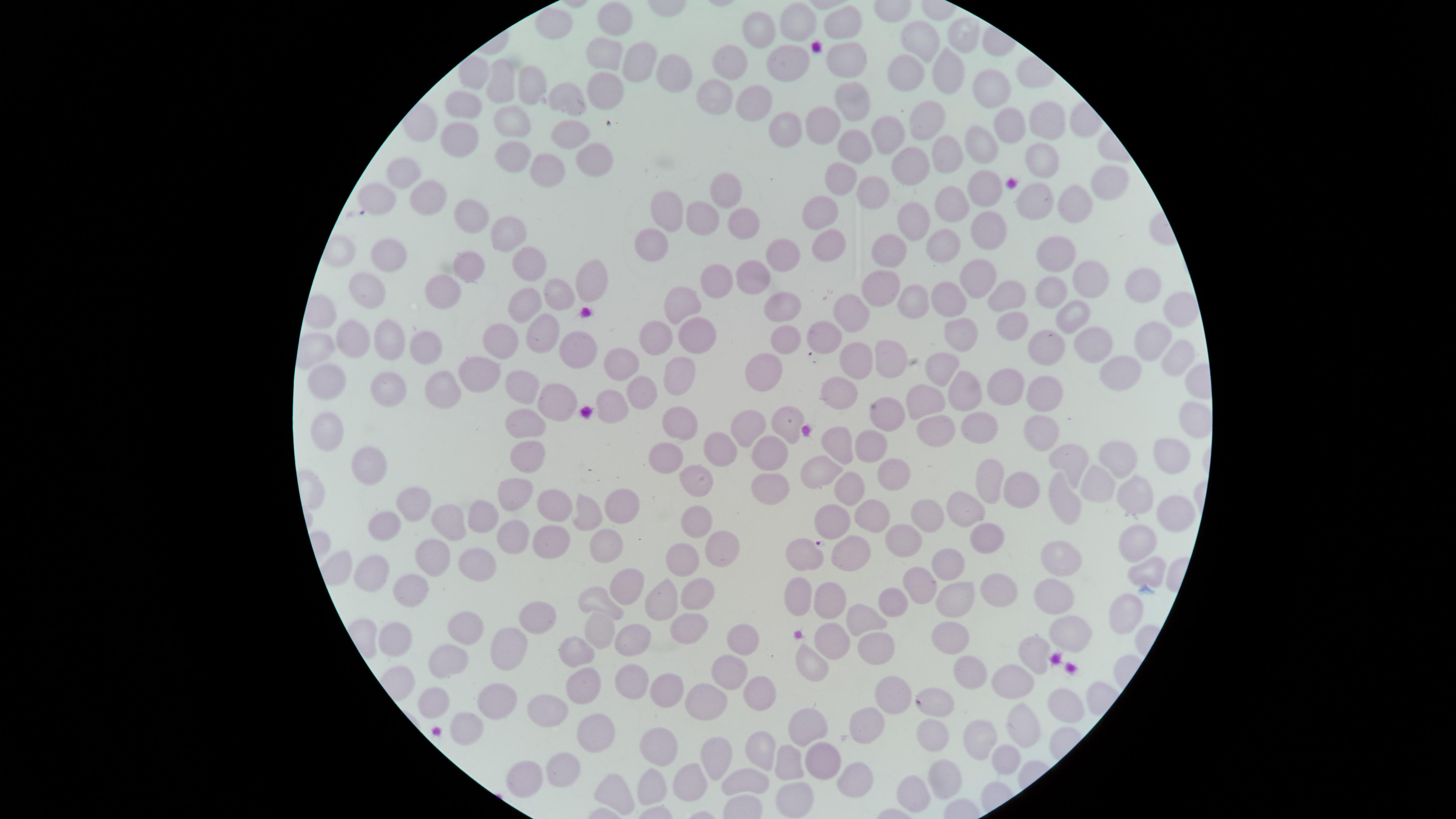 Approximate marker points as [x, y] in pixels. Uninfected red blood cells: [619, 19], [796, 21], [845, 22], [554, 27], [761, 29], [963, 32], [909, 47], [605, 57], [846, 57], [732, 60], [790, 60], [642, 63], [941, 69], [475, 75], [675, 75], [907, 75], [501, 84], [996, 87], [527, 88], [602, 91], [717, 91], [566, 96], [753, 104], [855, 106], [457, 109], [511, 117], [1039, 120], [929, 121], [827, 126], [1010, 126], [785, 127], [881, 128], [463, 136], [570, 137], [985, 145], [857, 147], [589, 155], [509, 157], [953, 157], [1042, 164], [916, 168], [415, 170], [546, 173], [1108, 181], [842, 183], [725, 187], [988, 188], [871, 189], [1040, 193], [430, 199], [952, 204], [1068, 205], [670, 206], [824, 216], [469, 217], [741, 219], [702, 221], [920, 224], [988, 224], [505, 233], [947, 244], [832, 245], [650, 246], [381, 247], [888, 251], [1053, 253], [783, 254], [531, 262], [468, 270], [1095, 275], [585, 281], [747, 281], [976, 281], [363, 285], [716, 286], [559, 288], [1136, 288], [1053, 290], [439, 291], [881, 291], [1009, 293], [917, 298], [948, 299], [681, 306], [518, 307], [783, 307], [1171, 307], [1066, 313], [855, 316], [1013, 325], [540, 331], [354, 332], [825, 333], [658, 336], [961, 336], [388, 340], [577, 340], [784, 340], [500, 341], [696, 342], [421, 344], [1152, 346], [1089, 348], [1046, 351], [852, 358], [618, 360], [888, 360], [1175, 360], [941, 368], [766, 370], [678, 374], [479, 377], [1122, 377], [324, 380], [519, 385], [961, 385], [1001, 385], [1044, 386], [390, 387], [642, 389], [439, 392], [839, 396], [560, 399], [612, 401], [928, 402], [886, 414], [785, 421], [674, 422], [745, 425], [321, 427], [526, 427], [1043, 427], [986, 429], [937, 431], [869, 448], [845, 449], [1172, 451], [729, 452], [768, 452], [1069, 457], [1118, 457], [528, 460], [663, 463], [373, 467], [821, 469], [893, 474], [990, 478], [1105, 481], [702, 482], [851, 487], [1023, 487], [773, 488], [1071, 493], [1142, 499], [626, 500], [516, 502], [415, 503], [968, 503], [552, 506], [587, 511], [1172, 513], [935, 514], [489, 517], [828, 517], [873, 519], [451, 521], [383, 522], [696, 527], [985, 537], [508, 540], [546, 540], [906, 540], [606, 542], [1134, 546], [717, 549], [851, 552], [799, 555], [1071, 558], [434, 560], [686, 561], [947, 564], [366, 567], [1140, 568], [478, 569], [629, 583], [916, 585], [415, 588], [1004, 592], [799, 593], [696, 594], [1054, 594], [896, 598], [605, 599], [961, 599], [668, 600], [834, 600], [538, 615], [1119, 616], [866, 617], [688, 624], [473, 627], [599, 628], [1066, 633], [395, 635], [735, 641], [955, 641], [879, 643], [828, 645], [632, 646], [506, 647], [1035, 651], [572, 656], [804, 661], [445, 663], [976, 675], [723, 677], [626, 681], [582, 683], [1016, 684], [666, 691], [756, 696], [492, 697], [940, 699], [1054, 701], [429, 702], [706, 702], [897, 702], [552, 704], [869, 716], [802, 726], [597, 728], [463, 730], [1023, 731], [934, 736], [977, 743], [660, 749], [757, 749], [708, 757], [1004, 758], [785, 759], [820, 759], [563, 761], [747, 774], [525, 775], [692, 779], [855, 781], [949, 782], [610, 786], [654, 787], [794, 794], [916, 798]. Image is 1456×819 pixels. Circular visible region. Photographed with a smartphone camera through the microscope eyepiece. Single field of view. Giemsa-stained preparation. Thin blood film. Presence: no malaria parasites identified.